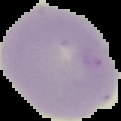
malaria_status: uninfected
image_type: cell region segmented out of the field of view; surrounding area masked to black
image_size: 121×121 pixels
preparation: thin blood film